Name the blood parasite species.
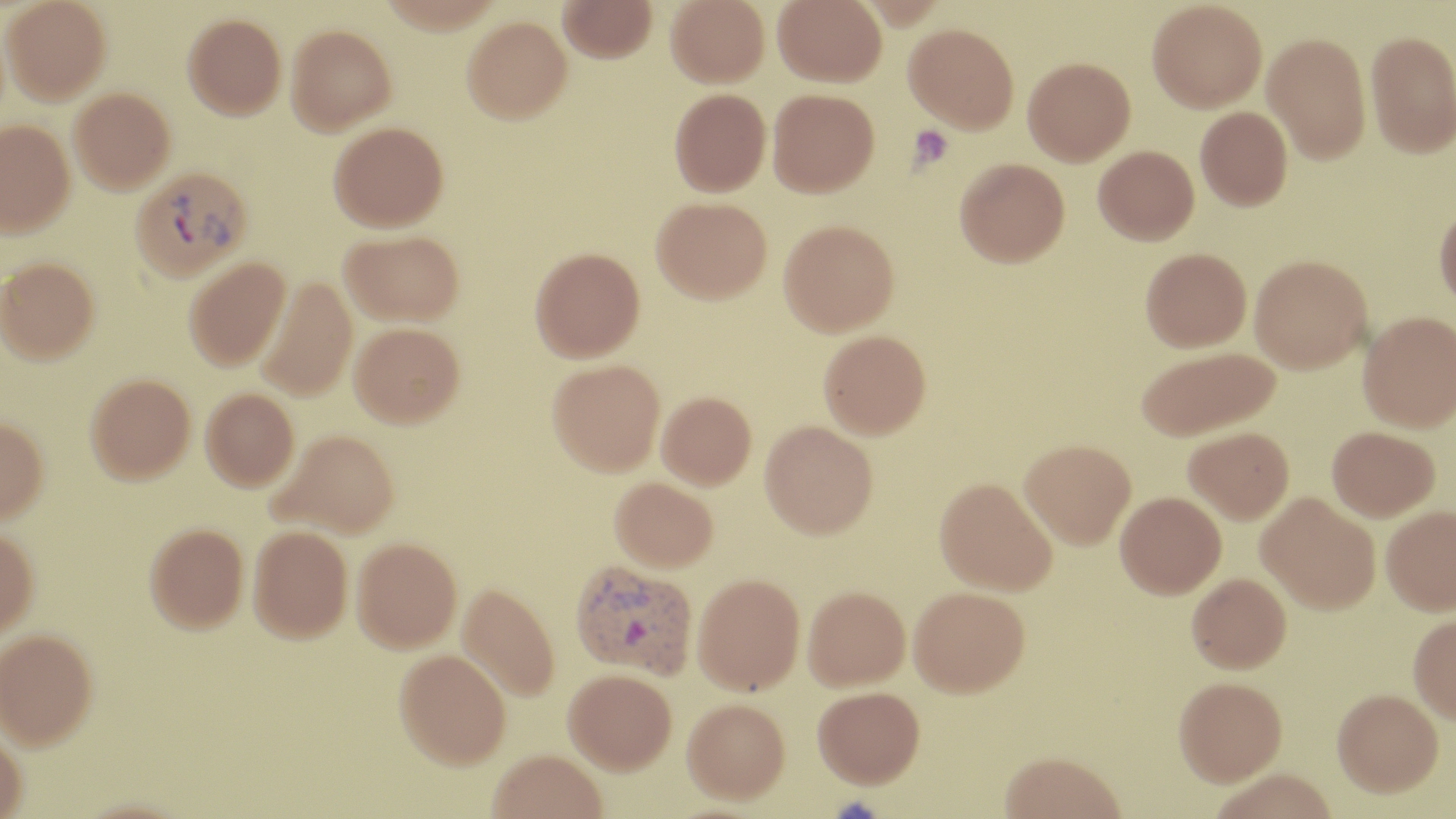

Plasmodium vivax.

Approximate bounding boxes as [x1, y1, x2, y2] in pixels. Uninfected red blood cell locations: [2, 0, 111, 104], [558, 0, 657, 63], [666, 0, 769, 87], [773, 0, 887, 87], [1147, 0, 1267, 113], [183, 13, 287, 119], [462, 16, 572, 123], [904, 23, 1019, 132], [286, 24, 396, 134], [1366, 29, 1456, 158], [1262, 32, 1371, 164], [1023, 57, 1135, 166], [69, 87, 175, 193], [669, 88, 771, 196], [768, 88, 879, 196], [1195, 106, 1292, 211], [0, 119, 75, 237], [329, 121, 448, 231], [1093, 145, 1199, 245], [955, 157, 1070, 266], [651, 197, 772, 303], [1434, 202, 1456, 310], [779, 219, 899, 336], [340, 229, 464, 326], [530, 246, 645, 362], [1140, 247, 1251, 352], [1249, 254, 1372, 373], [184, 256, 290, 371], [0, 257, 99, 363], [256, 277, 358, 401], [1358, 311, 1455, 432], [349, 322, 464, 427], [819, 329, 931, 438], [1136, 346, 1280, 441], [547, 359, 665, 475], [85, 373, 195, 483], [201, 388, 299, 491], [656, 391, 756, 489], [0, 416, 49, 523], [760, 421, 878, 538], [1183, 426, 1294, 523], [1327, 426, 1440, 521], [270, 429, 399, 538], [1020, 439, 1136, 548], [610, 477, 717, 572], [934, 477, 1057, 595], [1116, 491, 1226, 598], [1256, 493, 1380, 614], [1381, 504, 1456, 615], [145, 523, 249, 632], [248, 526, 352, 642], [0, 527, 39, 638], [351, 537, 462, 652], [1187, 572, 1291, 673], [693, 573, 805, 694], [457, 582, 560, 701], [803, 586, 910, 690], [909, 586, 1030, 696], [1408, 613, 1456, 725], [0, 628, 98, 749], [394, 648, 511, 768], [563, 668, 676, 773], [1173, 676, 1287, 786], [813, 686, 924, 787], [1332, 688, 1444, 797], [683, 697, 790, 802], [0, 728, 27, 819], [488, 750, 608, 819], [1000, 751, 1126, 819], [1208, 768, 1338, 819]. Platelet locations: [908, 125, 952, 169]. Plasmodium vivax-infected red blood cell locations: [129, 165, 252, 282], [569, 559, 698, 679]. Light microscopy. Image is 1456×819 pixels. Captured at 1000x magnification. Single field of view. Thin blood film. May-Grünwald-Giemsa stain.